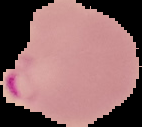

Result: Plasmodium parasites detected. The area outside the segmented cell region is set to black. From a thin blood film. Image is 142×127 pixels.